Assess the morphology of the erythrocytes.
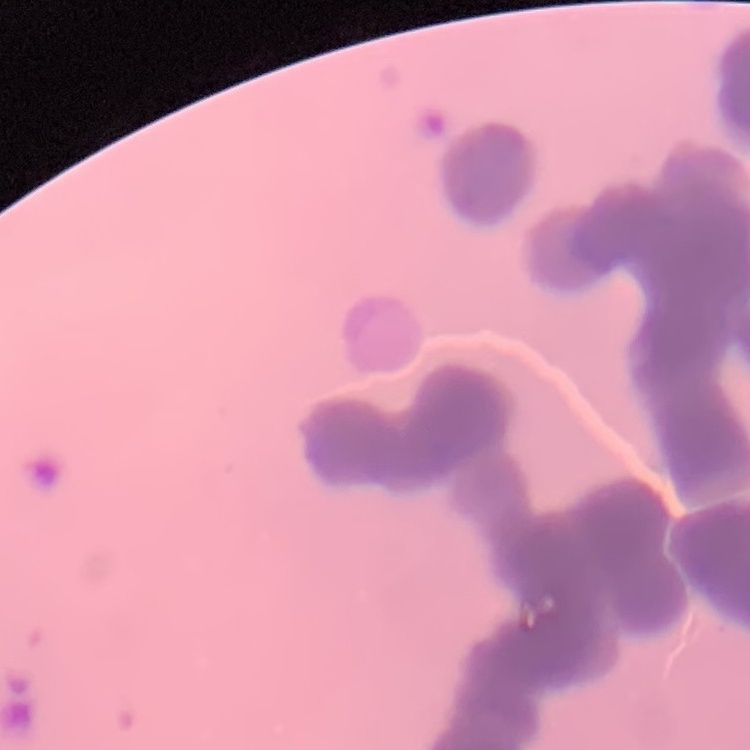
They show rouleaux formation.

Stained with either Field's or Giemsa. Square crop of a larger photomicrograph. Thin peripheral smear.